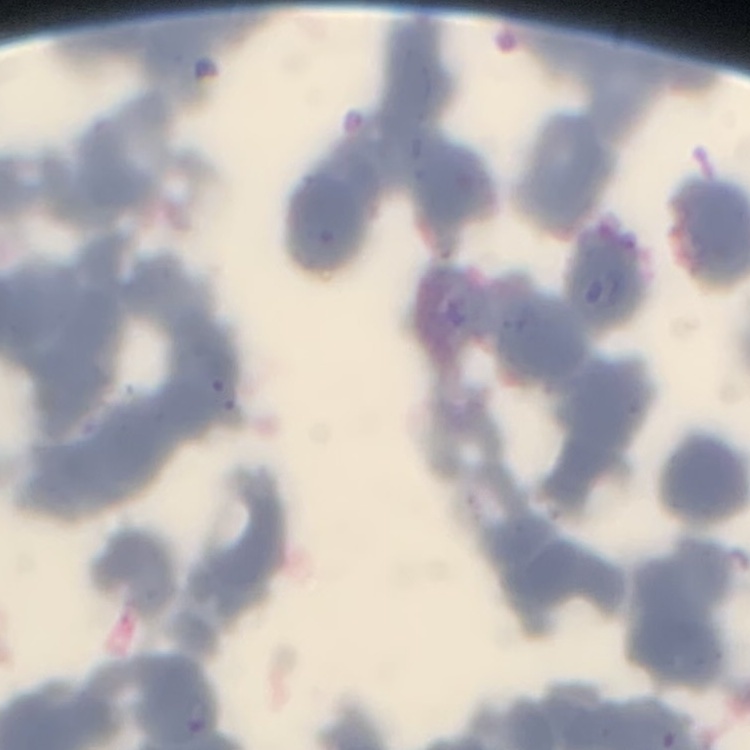
Summary:
  - Red blood cell morphology: rouleaux formation
  - Image type: one tile cut from a larger photomicrograph
  - Preparation: thin peripheral smear
  - Stain: Field's or Giemsa